Comment on the morphology of the erythrocytes.
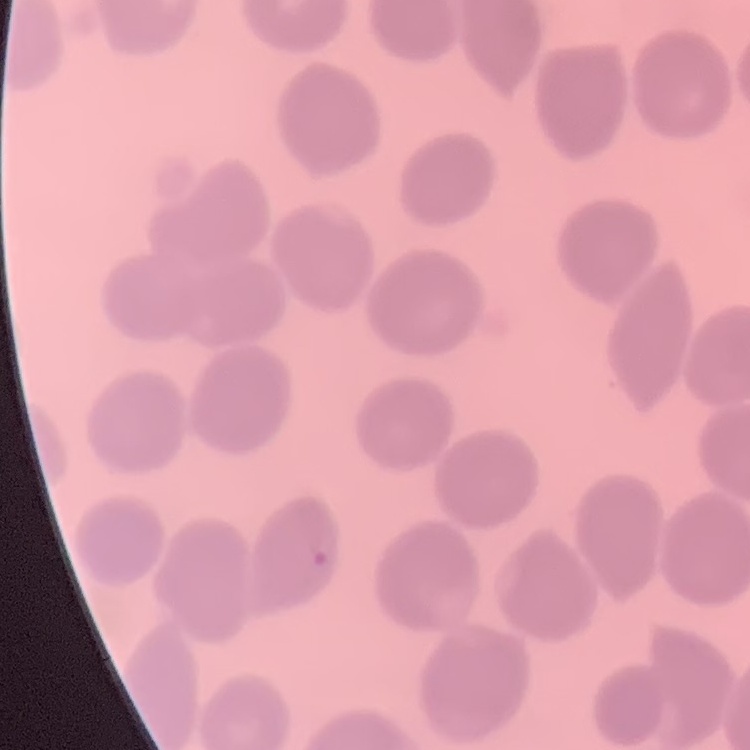
They show no rouleaux formation.

Summary:
  - Stain: Field's or Giemsa
  - Image type: one tile cut from a larger photomicrograph
  - Preparation: thin blood film